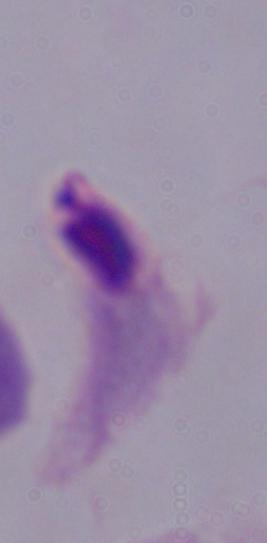
identification = trichomonad
modality = micrograph
magnification = 1000x